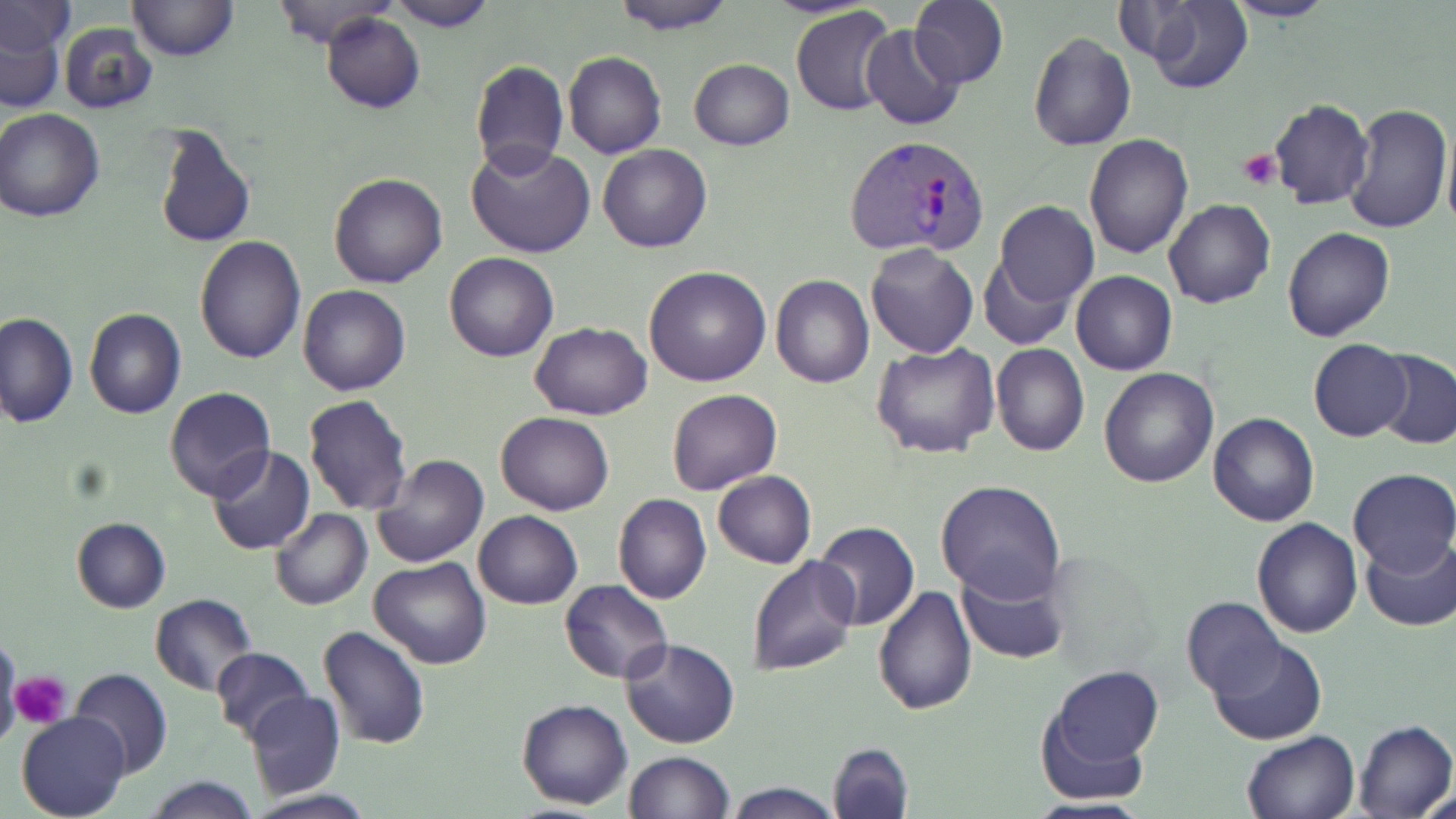
Approximate bounding boxes as [x1, y1, x2, y2] in pixels. Uninfected red blood cell locations: [127, 0, 237, 61], [270, 0, 396, 47], [384, 0, 497, 32], [611, 0, 739, 35], [1222, 0, 1336, 24], [909, 1, 1008, 88], [1132, 1, 1254, 93], [1, 3, 77, 56], [791, 6, 900, 116], [1, 12, 69, 111], [321, 12, 425, 114], [60, 22, 156, 113], [861, 26, 965, 131], [1027, 32, 1136, 152], [563, 51, 666, 158], [689, 58, 794, 151], [470, 61, 569, 176], [1268, 99, 1374, 209], [1344, 102, 1453, 236], [0, 109, 105, 222], [1442, 119, 1456, 241], [152, 121, 256, 250], [1083, 136, 1194, 258], [467, 143, 595, 258], [599, 144, 711, 252], [330, 173, 447, 289], [1164, 200, 1276, 309], [993, 201, 1099, 308], [1283, 228, 1395, 342], [194, 235, 306, 364], [865, 244, 978, 360], [445, 251, 558, 362], [978, 255, 1074, 350], [644, 266, 771, 387], [1071, 271, 1177, 375], [771, 276, 875, 389], [299, 285, 411, 397], [84, 308, 187, 420], [1, 312, 77, 428], [530, 322, 652, 418], [1308, 339, 1412, 440], [872, 343, 1001, 460], [992, 344, 1089, 457], [1374, 350, 1456, 450], [1099, 367, 1219, 487], [164, 387, 275, 501], [667, 388, 781, 495], [303, 394, 412, 514], [495, 411, 613, 515], [1208, 413, 1320, 526], [207, 446, 314, 555], [372, 454, 489, 568], [1348, 468, 1456, 574], [712, 471, 815, 569], [937, 480, 1067, 603], [614, 494, 712, 605], [271, 509, 372, 611], [473, 510, 582, 610], [71, 517, 171, 613], [1252, 518, 1363, 638], [814, 522, 921, 631], [1361, 534, 1456, 631], [748, 554, 860, 676], [369, 558, 491, 670], [957, 566, 1070, 664], [559, 580, 673, 683], [871, 585, 977, 716], [150, 594, 257, 695], [1182, 596, 1286, 700], [318, 626, 431, 750], [0, 635, 21, 748], [618, 637, 741, 749], [1207, 637, 1327, 745], [210, 646, 314, 742], [1038, 664, 1166, 790], [72, 668, 172, 780], [245, 691, 346, 800], [516, 697, 633, 810], [17, 712, 129, 819], [1354, 720, 1455, 819], [1242, 730, 1359, 819], [827, 742, 914, 819], [624, 751, 733, 819], [142, 775, 262, 818], [724, 780, 842, 818], [1423, 786, 1455, 819], [244, 790, 377, 819]. Plasmodium vivax-infected red blood cell locations: [847, 133, 989, 260]. Platelet locations: [1238, 148, 1280, 191], [11, 670, 70, 730]. Slide-level diagnosis: Plasmodium vivax. Optical microscopy. May-Grünwald-Giemsa stain. Thin blood smear. Image is 1456×819 pixels. 1000x magnification. One field of a larger specimen.